Classify this cell by malaria status.
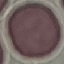
Uninfected.

Summary:
  - Capture: smartphone through the microscope eyepiece
  - Preparation: thin blood smear
  - Stain: Giemsa
  - Image type: cell patch, automatically extracted from a larger field of view and resized to 64 × 64 pixels